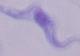

Summary:
  - Identification: trypanosome
  - Magnification: 1000x
  - Modality: micrograph